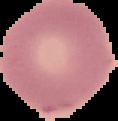
Result: negative for Plasmodium parasites. Image is 118×121 pixels. Cell region segmented out of the field of view; the surrounding area is masked to black. From a thin blood film.